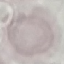 Malaria status: uninfected. Photographed with a smartphone camera at the microscope eyepiece. Automatically extracted cell patch, resized to 64 × 64 pixels. Thin smear of blood. Giemsa-stained preparation.